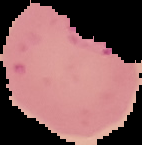 Malaria status: parasitized. Image is 142×145 pixels. Segmented cell region on a black background. From a thin blood film.